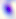

magnification = 400x
modality = micrograph
identification = Toxoplasma gondii